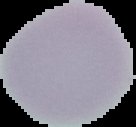
result = no malaria parasites detected
image type = segmented cell region with the area outside set to black
image size = 136×127 pixels
preparation = thin blood film